Classify this cell by malaria status.
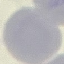

Uninfected.

Summary:
  - Image type: automatically extracted cell patch, resized to 64 × 64 pixels
  - Capture: smartphone through the microscope eyepiece
  - Preparation: thin blood smear
  - Stain: Giemsa